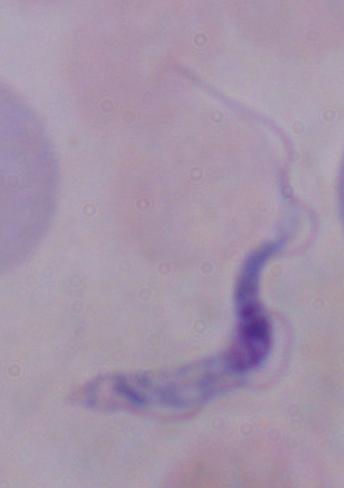
magnification = 1000x
modality = photomicrograph
identification = trypanosome